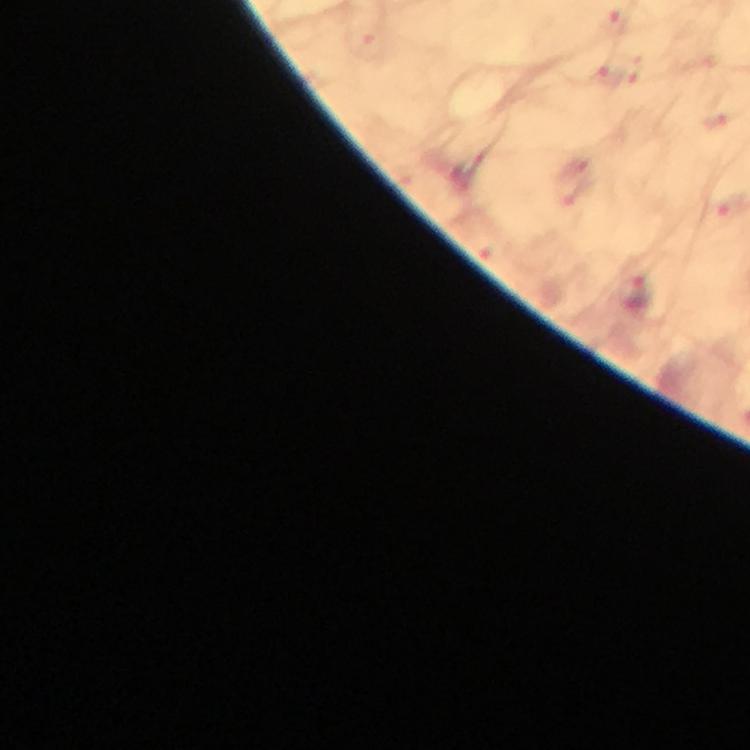
Approximate centers as [x, y] in pixels. Malaria parasite locations: [636, 292]. Thick smear. Photographed with a smartphone mounted on the microscope. Cropped region of a single field of view. Immersion oil was used. From a diagnostic examination for malaria. At 100x magnification. Image is 750×750 pixels. Giemsa-stained preparation.